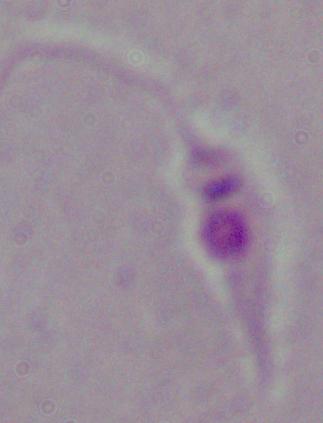
modality = photomicrograph
identification = Leishmania
magnification = 1000x